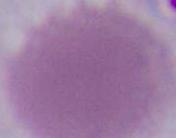
Summary:
  - Magnification: 1000x
  - Identification: erythrocyte
  - Modality: photomicrograph